Classify this cell by malaria status.
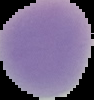
Uninfected.

Summary:
  - Image type: segmented cell region on a black background
  - Preparation: thin blood smear
  - Image size: 94×100 pixels